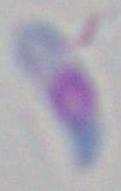
Summary:
  - Identification: Toxoplasma gondii
  - Modality: photomicrograph
  - Magnification: 1000x